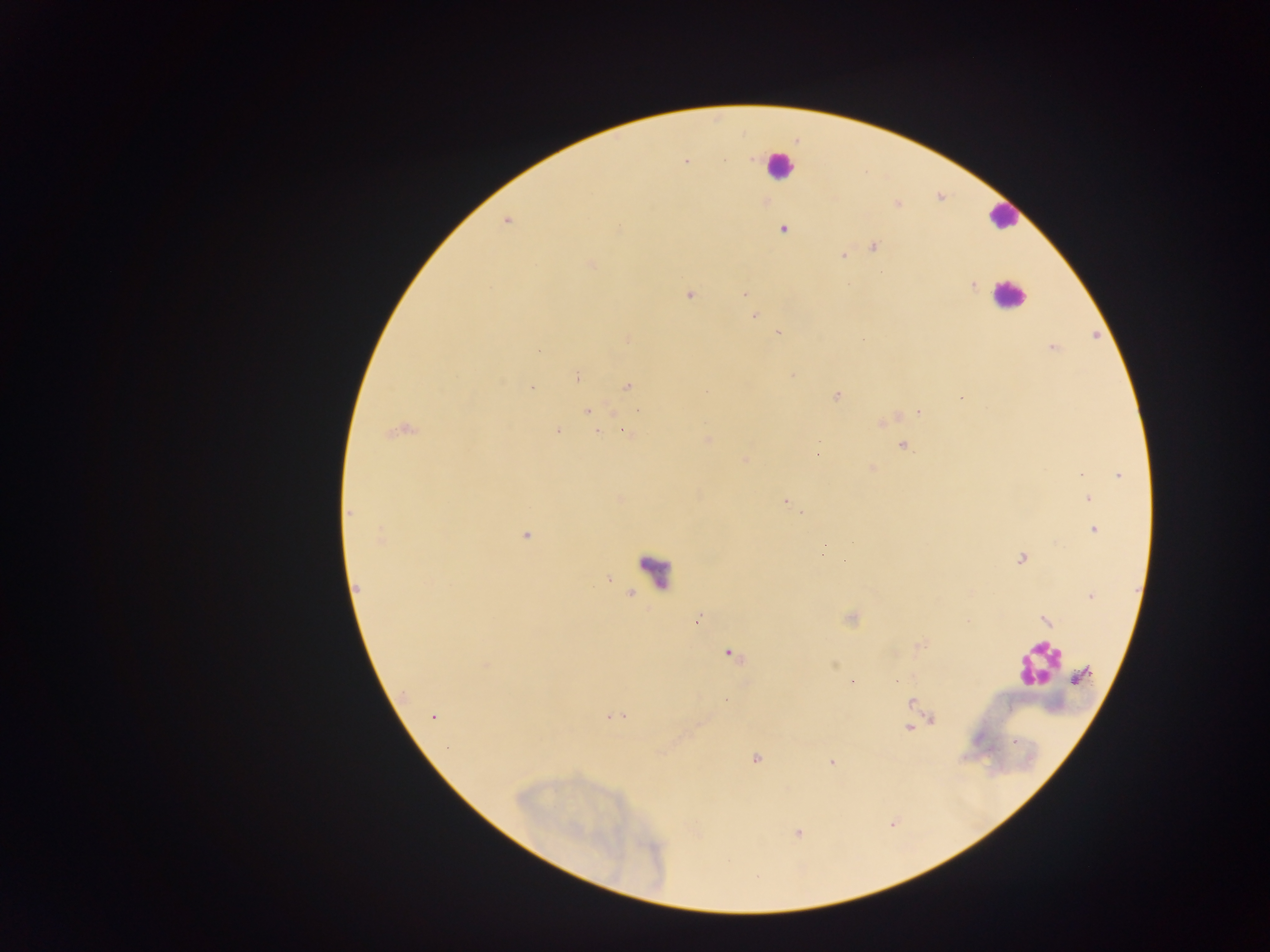

Approximate centers as [x, y] in pixels.
Summary:
  - Leukocyte locations (subset; some below the resolvable size): [777, 166], [1002, 216], [1008, 296], [657, 570], [1036, 664]
  - Malaria parasite locations: [724, 159], [685, 161], [619, 227], [783, 229], [874, 246], [842, 255], [591, 264], [972, 285], [689, 294], [746, 294], [754, 317], [778, 332], [1052, 347], [792, 375], [578, 377], [627, 386], [531, 388], [707, 391], [836, 396], [961, 397], [587, 411], [919, 412], [557, 430], [623, 430], [401, 431], [598, 431], [708, 440], [819, 445], [902, 446], [818, 455], [745, 460], [872, 468], [1081, 475], [1119, 476], [1089, 499], [786, 501], [349, 513], [800, 514], [1093, 530], [525, 535], [381, 537], [821, 554], [1020, 559], [358, 587], [1091, 596], [1045, 620], [697, 621], [920, 645], [729, 654], [486, 666], [1081, 675], [896, 681], [852, 683], [405, 693], [726, 700], [912, 702], [433, 717], [616, 717], [933, 719], [908, 728], [756, 759], [831, 762]
  - Preparation: thick blood film
  - Field of view: single
  - Image size: 1270×952 pixels
  - Capture: mobile-phone photograph through a microscope
  - Country: Ghana